Classify this cell by malaria status.
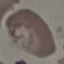
Parasitized.

{
  "preparation": "thin blood film",
  "capture": "smartphone camera at the microscope eyepiece",
  "image_type": "automatically extracted cell patch, resized to 64 × 64 pixels",
  "stain": "Giemsa"
}